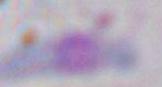 1000x magnification. Micrograph. Toxoplasma gondii is seen.